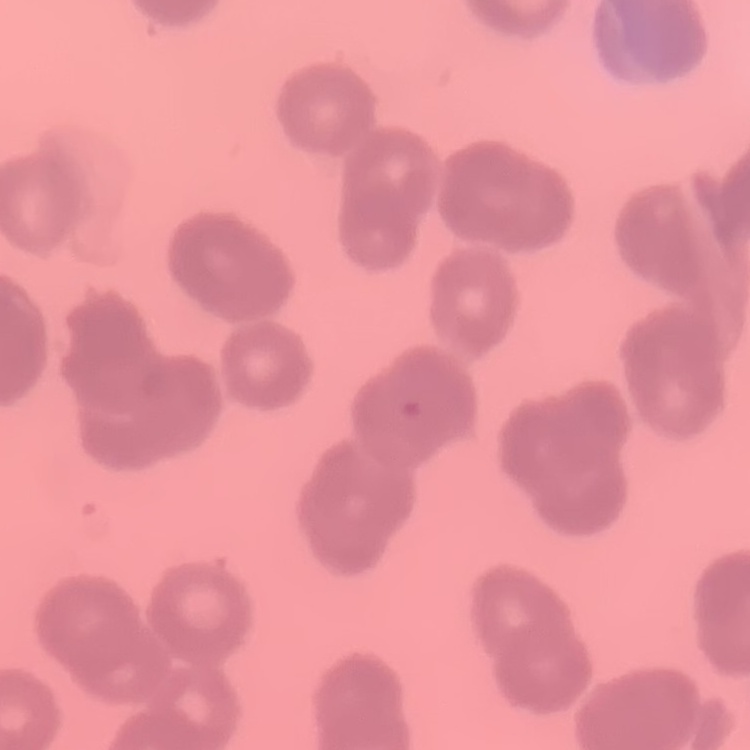

Summary:
  - Erythrocyte morphology: rouleaux formation
  - Image type: one tile cut from a larger photomicrograph
  - Preparation: thin blood smear
  - Stain: Field's or Giemsa